Classify this cell by malaria status.
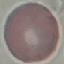

Uninfected.

capture = smartphone camera at the microscope eyepiece
stain = Giemsa
image type = cell patch, automatically extracted from a larger field of view and resized to 64 × 64 pixels
preparation = thin smear